Comment on the morphology of the erythrocytes.
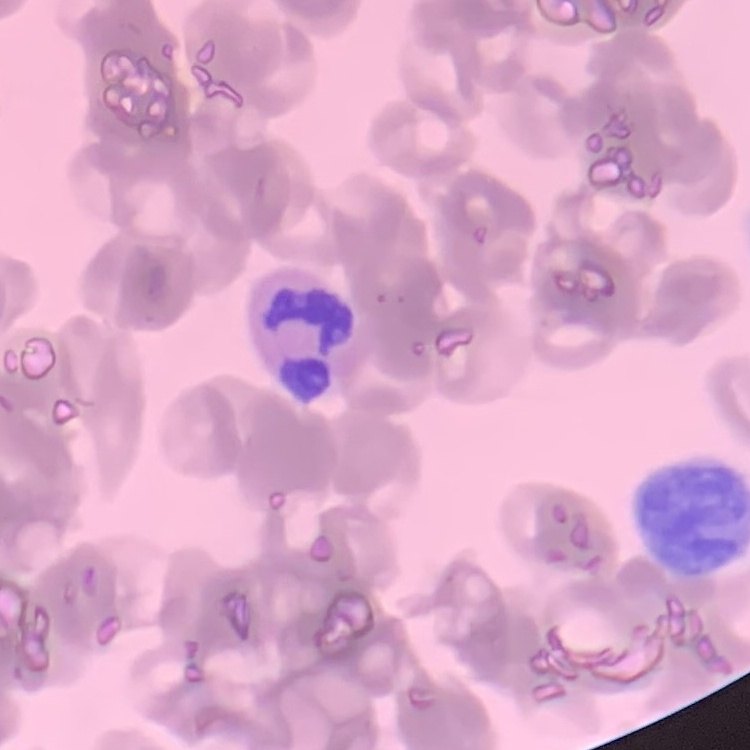
Rouleaux formation.

Square crop of a larger photomicrograph. Thin blood film. Field's or Giemsa stain.